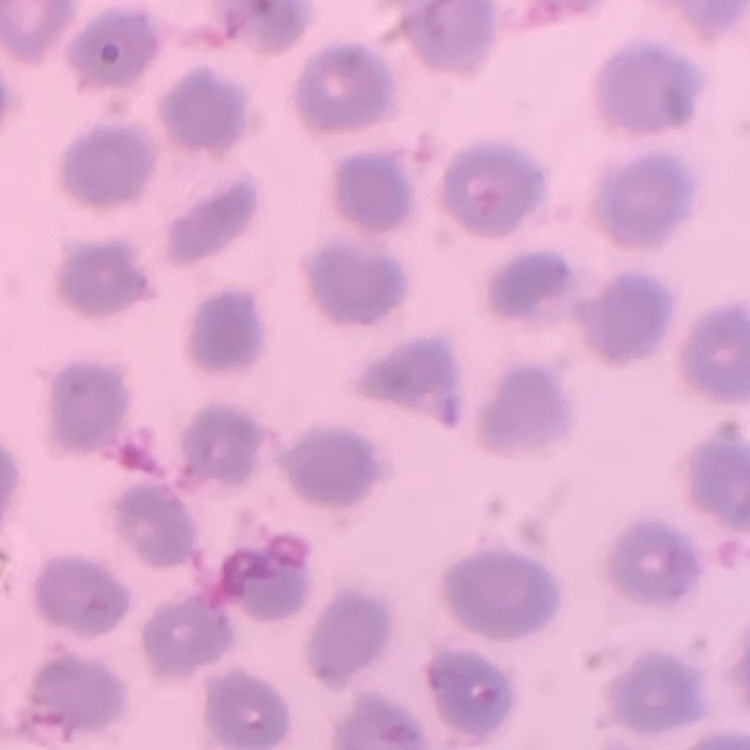

The erythrocytes show no rouleaux formation. Stained with either Field's or Giemsa. Thin blood smear. One tile cut from a larger photomicrograph.